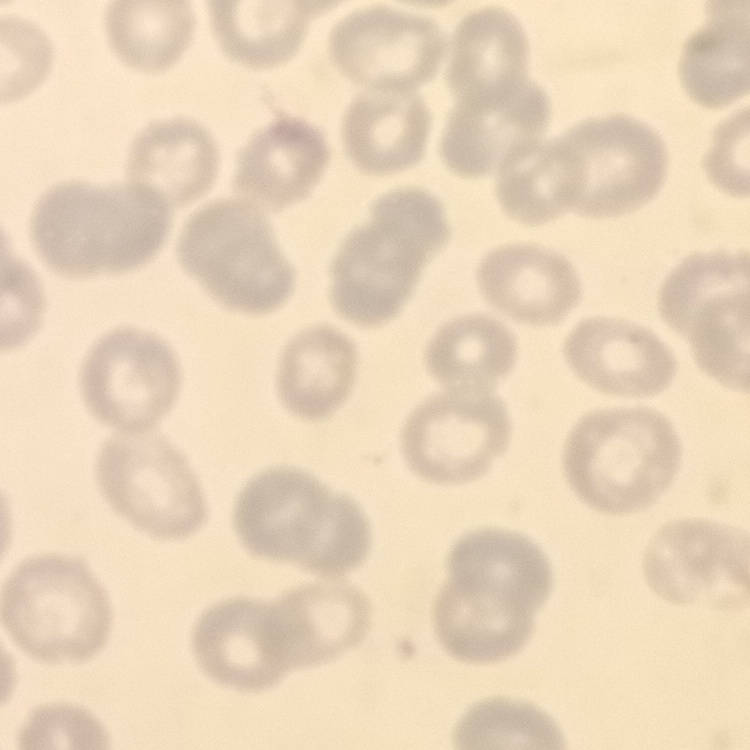

Summary:
  - Red blood cell morphology: no rouleaux formation
  - Preparation: thin blood smear
  - Stain: Field's or Giemsa
  - Image type: one tile cut from a larger photomicrograph